Comment on the morphology of the erythrocytes.
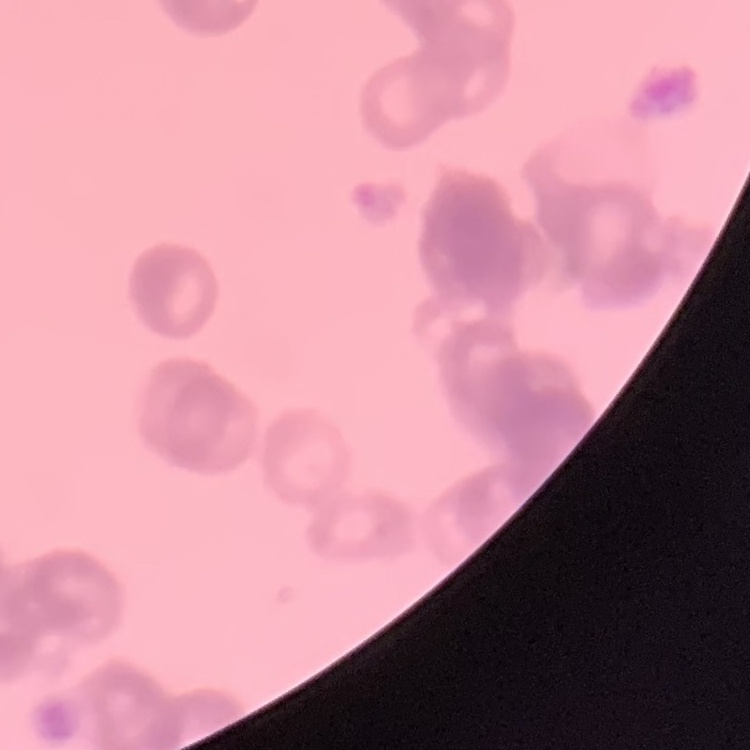
Rouleaux formation.

Field's or Giemsa stain. Thin peripheral smear. One tile cut from a larger photomicrograph.